Comment on the morphology of the erythrocytes.
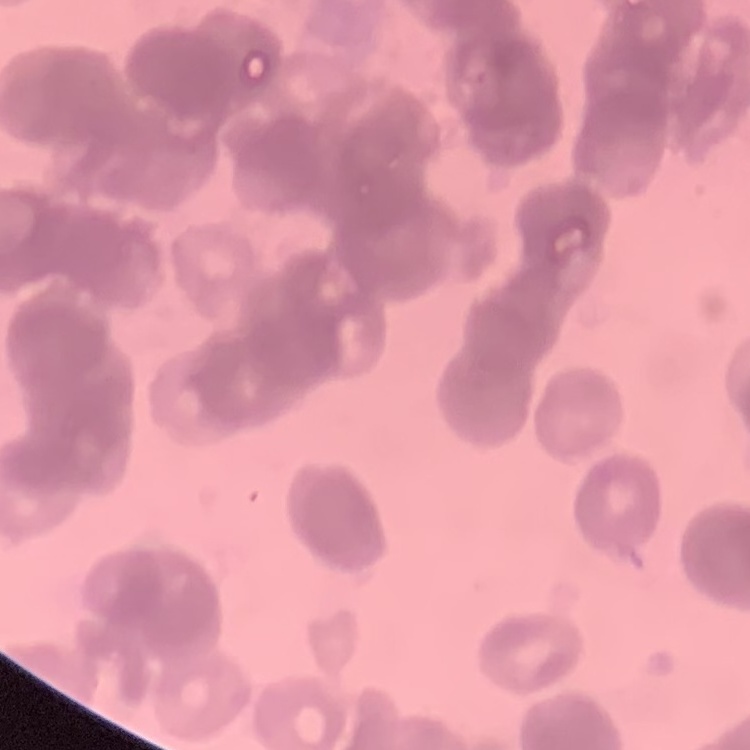
They show rouleaux formation.

Thin peripheral smear. Square crop of a larger photomicrograph. Stained with either Field's or Giemsa.